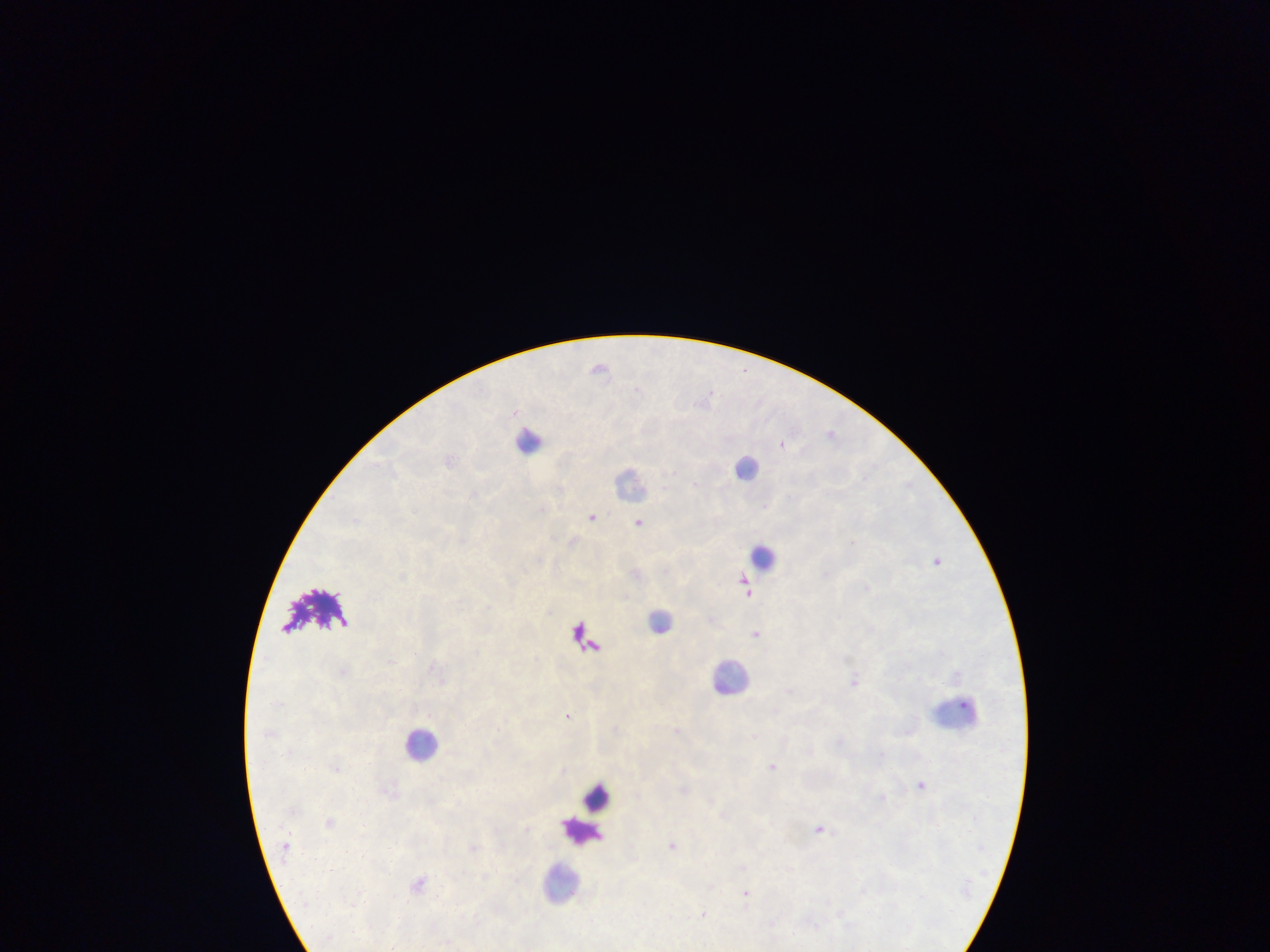

Approximate centers as x y in pixels. Plasmodium parasite locations: 600 367; 832 432; 782 442; 472 494; 593 517; 639 522; 851 542; 748 591; 756 633; 854 681; 790 691; 568 715; 677 730; 773 765; 921 784; 820 828; 673 845; 746 892; 703 914. Leukocyte locations: 529 439; 745 467; 631 482; 764 556; 661 620; 731 676; 951 714; 420 744; 597 797; 580 830; 559 882. Photographed through a microscope with a mobile-phone camera. Thick blood smear. Collected in Ghana. Image is 1270×952 pixels. One field of view.